Give the position of every malaria parasite and every leukocyte.
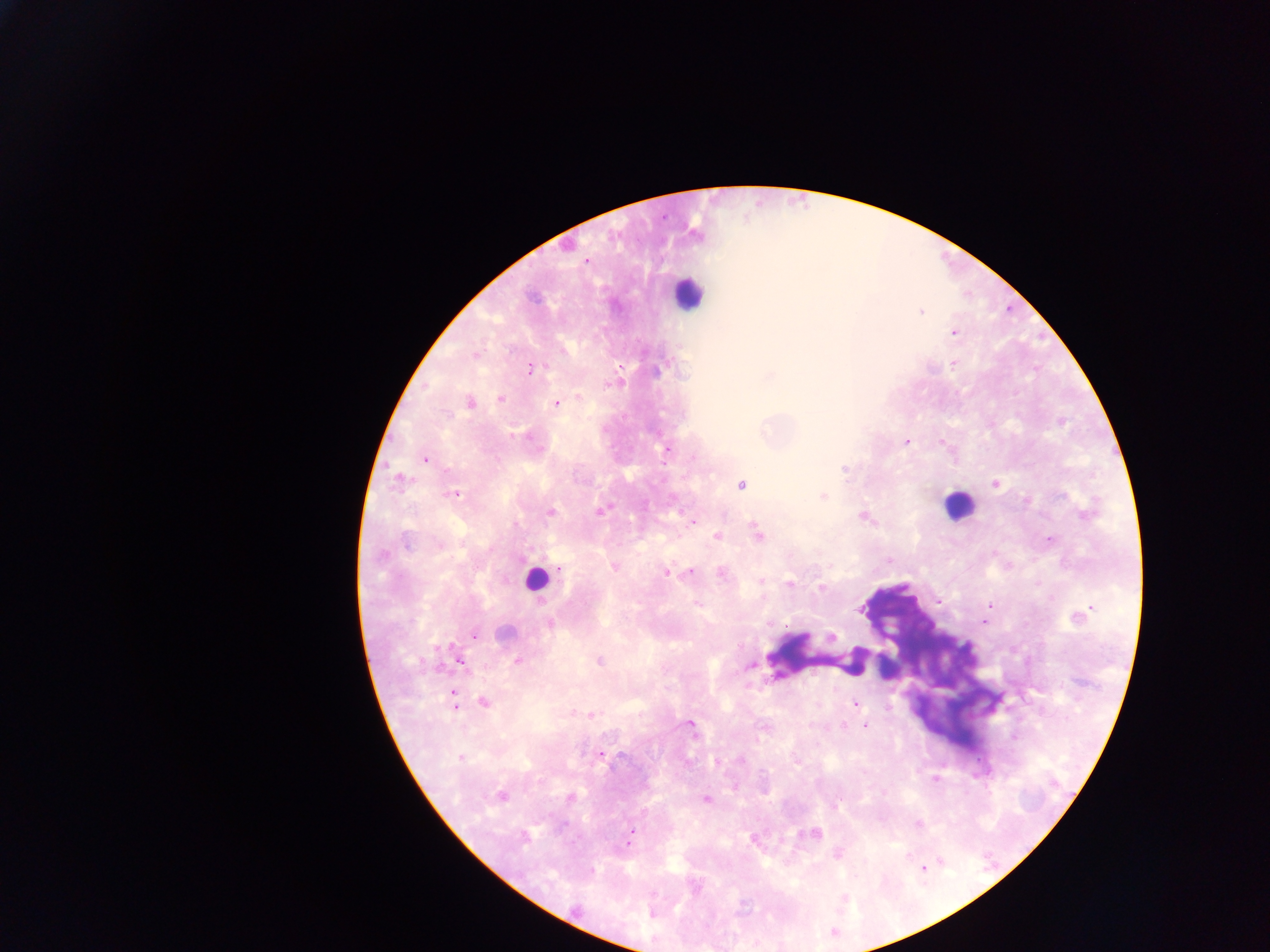
Approximate centers as (x, y) in pixels.
Malaria parasites: (567, 245), (586, 261), (920, 311), (954, 332), (474, 354), (953, 362), (530, 368), (500, 398), (469, 402), (556, 403), (906, 440), (941, 441), (667, 449), (424, 459), (398, 479), (740, 484), (995, 484), (454, 494), (822, 496), (601, 510), (550, 512), (864, 516), (693, 521), (756, 534), (716, 536), (1049, 539), (614, 566), (559, 567), (690, 570), (665, 572), (721, 572), (760, 580), (789, 584), (821, 587), (938, 601), (989, 605), (1092, 607), (1084, 612), (983, 623), (550, 624), (474, 634), (831, 637), (459, 660), (517, 660), (598, 661), (750, 664), (452, 695), (483, 701), (856, 703), (590, 715), (689, 724), (865, 725), (599, 755), (461, 757), (716, 761), (934, 779), (734, 787), (501, 795), (570, 798), (706, 799), (630, 832), (813, 833), (754, 838), (628, 839), (837, 853), (922, 868), (652, 913).
Leukocytes: (687, 294), (957, 506), (535, 578).

Summary:
  - Field of view: single
  - Capture: mobile-phone photograph through a microscope
  - Country: Ghana
  - Preparation: thick blood smear
  - Image size: 1270×952 pixels